Classify this cell by malaria status.
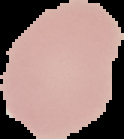

Uninfected.

{
  "image_type": "segmented cell region with the area outside set to black",
  "preparation": "thin blood smear",
  "image_size": "124×139 pixels"
}